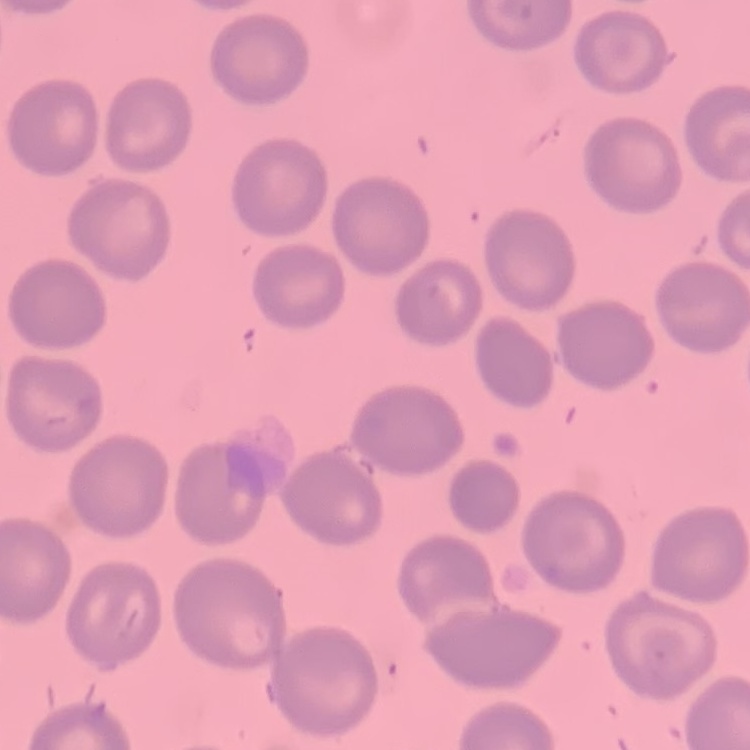
Summary:
  - Red blood cell morphology: no rouleaux formation
  - Preparation: thin blood smear
  - Image type: square crop of a larger photomicrograph
  - Stain: Field's or Giemsa